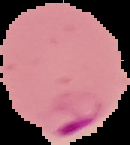

Summary:
  - Malaria status: parasitized
  - Image size: 130×145 pixels
  - Image type: cell region segmented out of the field of view; surrounding area masked to black
  - Preparation: thin blood smear